Classify this cell by malaria status.
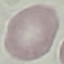
Uninfected.

Giemsa stain. Thin blood film. Photographed with a smartphone camera at the microscope eyepiece. Cell patch, automatically extracted from a larger field of view and resized to 64 × 64 pixels.